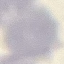

Result: no malaria parasites seen. Automatically extracted cell patch, resized to 64 × 64 pixels. Thin blood smear. Photographed with a smartphone camera at the microscope eyepiece. Giemsa stain.